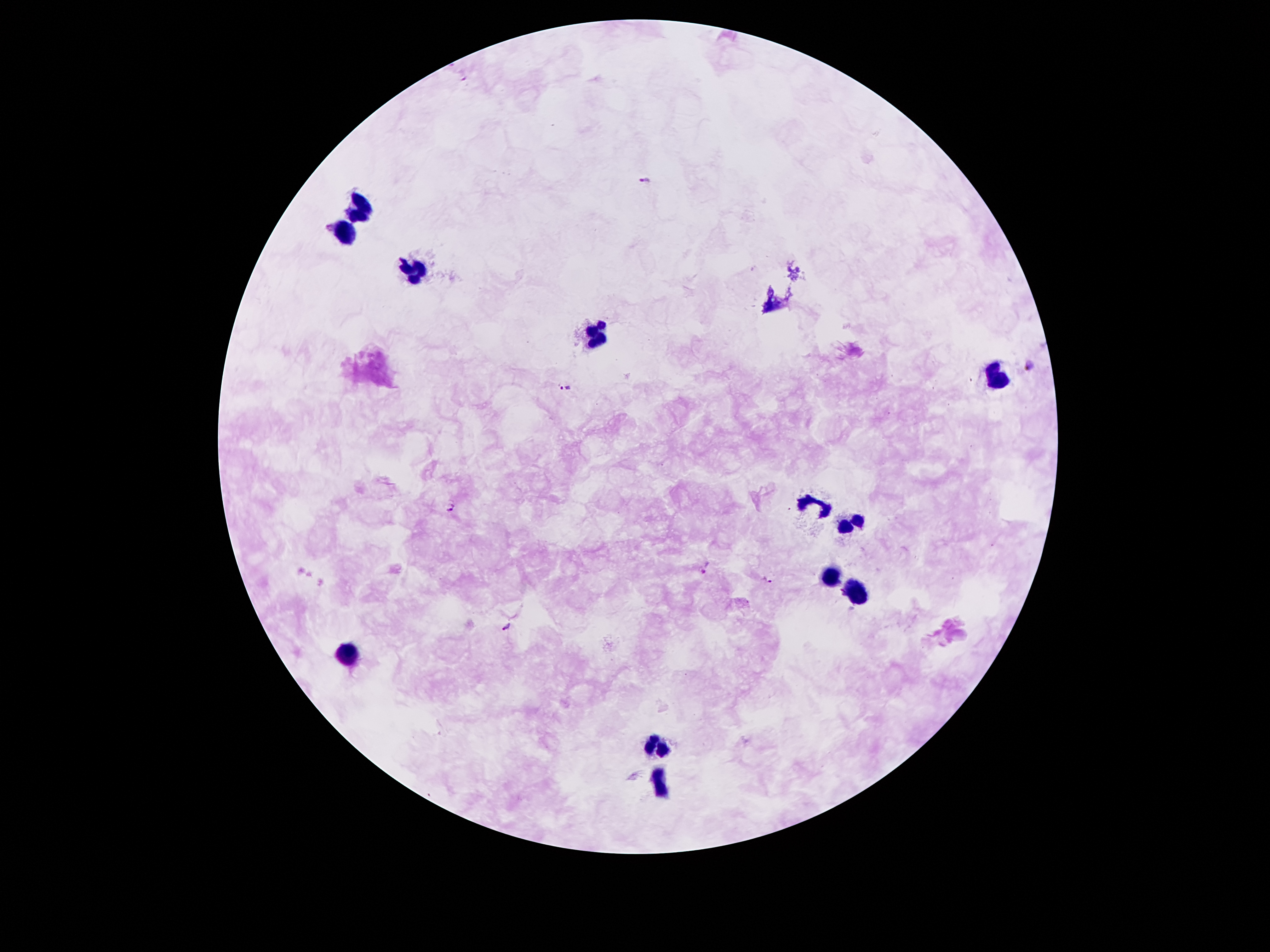

coordinate format = approximate object centers, in pixels from the top-left corner
leukocyte locations = (x=367, y=204), (x=346, y=226), (x=412, y=269), (x=593, y=338), (x=997, y=380), (x=814, y=505), (x=850, y=519), (x=829, y=576), (x=856, y=591), (x=352, y=655), (x=659, y=744), (x=656, y=784)
malaria parasite locations = (x=645, y=180), (x=1032, y=364), (x=565, y=389), (x=450, y=506), (x=705, y=569), (x=768, y=579), (x=507, y=626)
image size = 1270×952 pixels
field of view = one from this slide
patient malaria status = positive for Plasmodium falciparum
magnification = 100x
capture = smartphone through the microscope eyepiece
preparation = thick blood smear
stain = Giemsa